Classify this cell by malaria status.
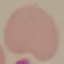

It is uninfected.

stain = Giemsa
image type = cell patch, automatically extracted from a larger field of view and resized to 64 × 64 pixels
preparation = thin blood film
capture = smartphone through the microscope eyepiece